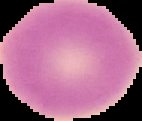
Summary:
  - Image type: cell region segmented out of the field of view; surrounding area masked to black
  - Malaria status: uninfected
  - Preparation: thin blood smear
  - Image size: 142×121 pixels